Locate every Plasmodium ovale-infected red blood cell.
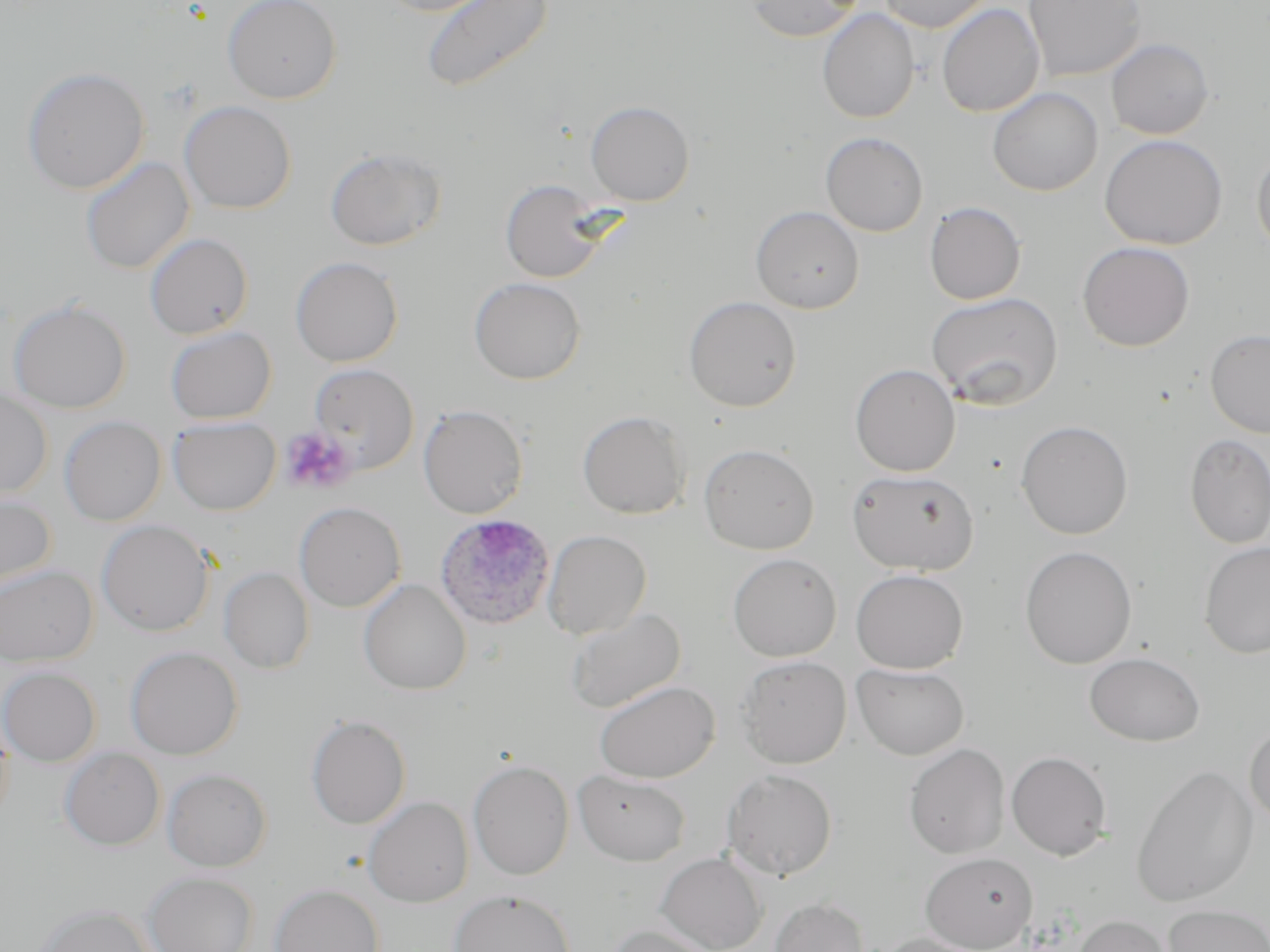
Approximate bounding boxes as (x1, y1, x2, y2) in pixels.
Plasmodium ovale-infected red blood cells: (435, 514, 556, 629).

Summary:
  - Uninfected red blood cell locations: (222, 0, 341, 103), (373, 0, 502, 16), (420, 0, 554, 94), (877, 0, 991, 33), (1023, 0, 1145, 82), (744, 1, 862, 42), (937, 3, 1044, 117), (817, 9, 920, 124), (1106, 38, 1214, 140), (22, 66, 149, 195), (987, 87, 1103, 196), (179, 100, 296, 214), (585, 100, 695, 206), (820, 132, 929, 236), (1099, 134, 1228, 250), (325, 146, 447, 251), (1251, 146, 1270, 257), (80, 156, 194, 275), (499, 179, 612, 283), (924, 201, 1026, 305), (750, 205, 865, 313), (144, 232, 253, 339), (1077, 241, 1195, 351), (290, 257, 403, 367), (468, 277, 585, 384), (926, 292, 1063, 411), (683, 296, 802, 412), (8, 299, 132, 413), (165, 326, 276, 424), (1205, 329, 1270, 437), (308, 363, 419, 473), (850, 364, 960, 476), (0, 388, 53, 500), (418, 404, 528, 519), (577, 410, 691, 519), (59, 416, 166, 526), (168, 417, 280, 515), (1015, 420, 1134, 540), (1184, 433, 1270, 548), (698, 443, 819, 554), (846, 469, 979, 576), (0, 492, 56, 591), (294, 502, 406, 612), (97, 520, 214, 637), (543, 529, 651, 639), (1198, 542, 1270, 659), (1019, 545, 1137, 669), (727, 553, 842, 661), (0, 564, 98, 666), (219, 567, 315, 673), (850, 568, 968, 673), (358, 578, 472, 695), (565, 607, 685, 714), (125, 646, 243, 759), (1083, 652, 1206, 746), (736, 655, 852, 768), (852, 663, 969, 760), (0, 666, 101, 766), (593, 680, 719, 783), (306, 714, 410, 829), (0, 716, 14, 826), (1245, 723, 1270, 830), (904, 743, 1010, 859), (59, 747, 165, 850), (1006, 751, 1112, 860), (468, 760, 574, 880), (1130, 764, 1259, 908), (162, 767, 272, 871), (722, 768, 838, 880), (573, 769, 691, 866), (363, 796, 473, 907), (655, 852, 767, 952), (920, 852, 1037, 952), (143, 871, 259, 952), (269, 883, 384, 952), (449, 889, 576, 952), (769, 897, 870, 952), (33, 903, 156, 952), (1162, 904, 1270, 952), (1071, 914, 1176, 952), (604, 924, 718, 952), (876, 933, 988, 952)
  - Platelet locations: (280, 426, 359, 495)
  - Slide-level diagnosis: Plasmodium ovale
  - Field of view: one of a larger specimen
  - Image size: 1270×952 pixels
  - Preparation: thin blood smear
  - Magnification: 1000x
  - Stain: May-Grünwald-Giemsa
  - Modality: optical microscopy